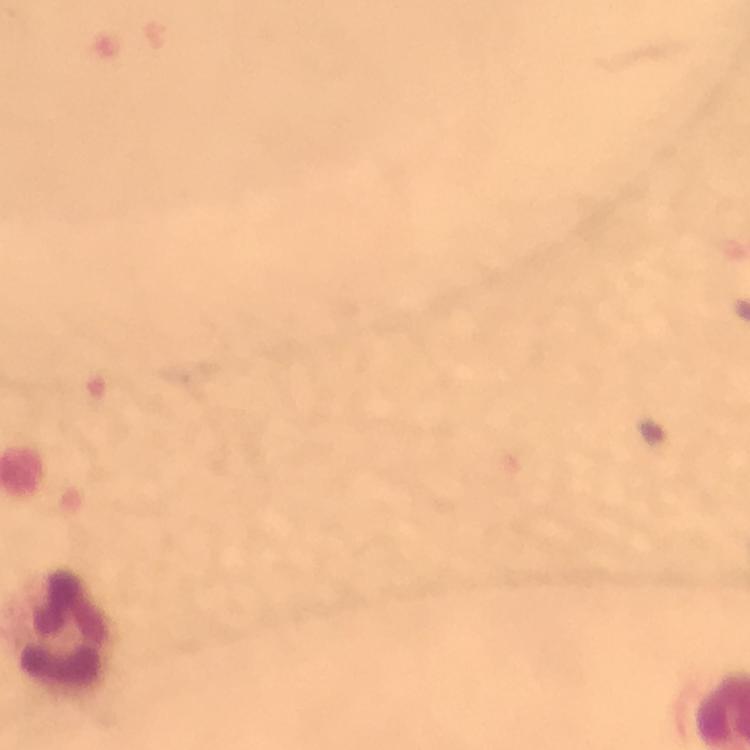

Approximate object centers, in pixels from the top-left corner.
Summary:
  - Leukocyte locations: (x=61, y=632)
  - Preparation: thick blood film
  - Cropped from: one field of view
  - Context: from a malaria diagnostic workup
  - Immersion oil: applied
  - Magnification: 100x
  - Malaria parasites: none detected
  - Capture: smartphone camera through the microscope
  - Stain: Giemsa
  - Image size: 750×750 pixels